Outline each blood parasite and name the species.
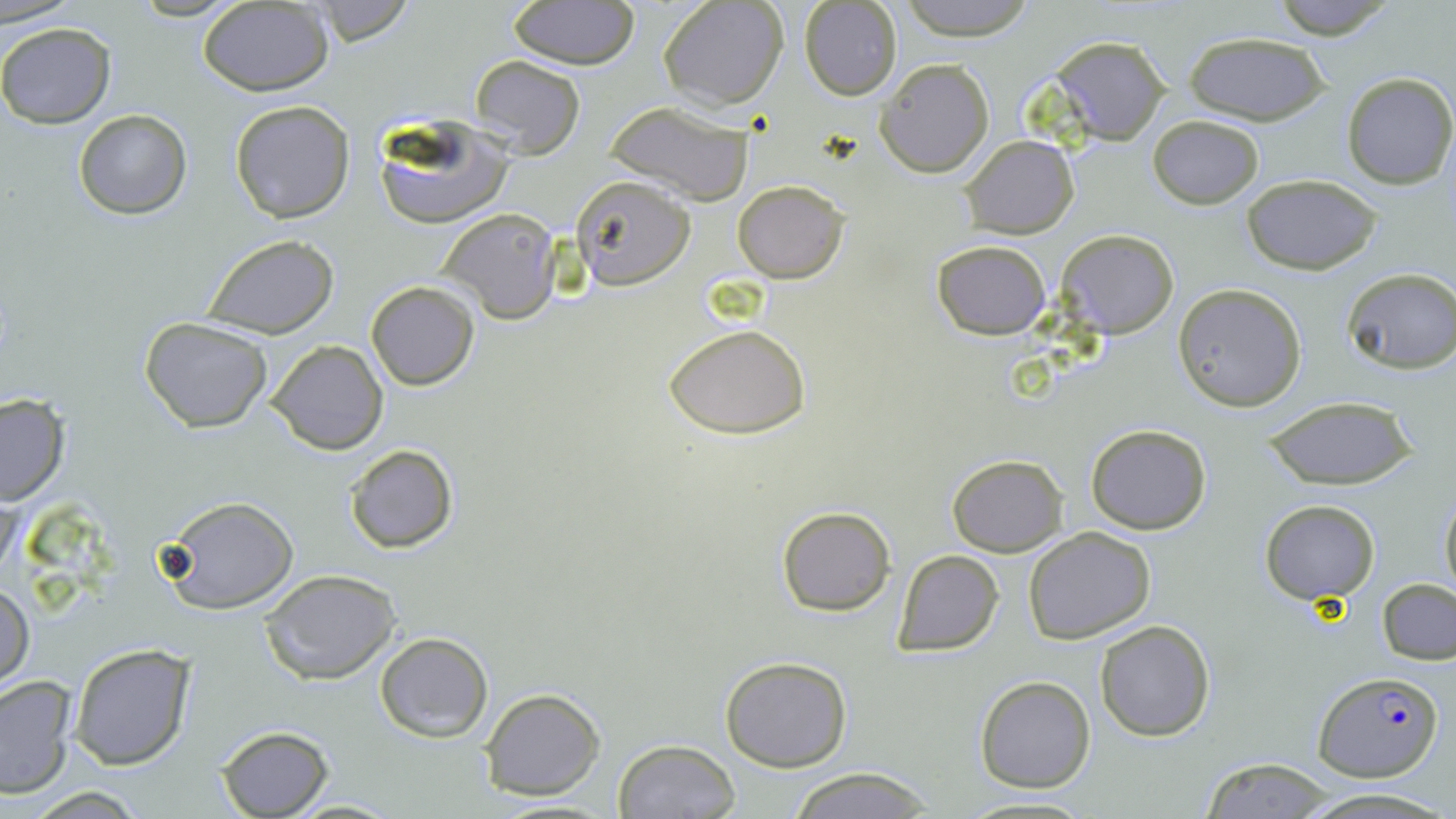

Approximate bounding boxes as (x1,y1)-(x2,y2) corner pairs in pixels.
Plasmodium falciparum-infected red blood cells: (1314,671)-(1444,782).
No Plasmodium ovale, Plasmodium malariae, Plasmodium vivax, Babesia divergens, or Trypanosoma brucei observed.

Summary:
  - Uninfected red blood cell locations: (3,0)-(79,26), (658,0)-(788,110), (896,0)-(1038,41), (1269,0)-(1398,40), (508,1)-(639,70), (798,1)-(902,99), (196,3)-(334,95), (0,22)-(115,128), (1182,33)-(1330,125), (1051,35)-(1171,144), (469,53)-(586,157), (874,58)-(995,178), (1340,71)-(1455,190), (229,99)-(356,223), (603,99)-(757,206), (73,108)-(192,221), (372,114)-(512,230), (1147,114)-(1264,208), (961,135)-(1078,237), (1241,174)-(1380,275), (572,175)-(696,289), (733,181)-(849,283), (438,208)-(562,324), (1057,229)-(1178,338), (202,235)-(340,338), (932,240)-(1051,338), (1342,269)-(1456,373), (366,281)-(480,391), (1173,284)-(1306,412), (139,316)-(274,433), (665,324)-(811,439), (268,340)-(386,455), (0,394)-(69,505), (1261,395)-(1419,490), (1086,423)-(1211,533), (344,443)-(458,554), (946,454)-(1067,557), (1439,483)-(1456,597), (156,494)-(299,614), (1259,499)-(1380,604), (775,505)-(897,617), (1022,527)-(1155,645), (893,549)-(1004,658), (260,569)-(399,684), (1378,578)-(1456,664), (1,582)-(35,692), (1095,619)-(1216,740), (374,631)-(493,742), (70,642)-(194,769), (719,655)-(852,772), (0,673)-(78,798), (974,675)-(1096,792), (479,687)-(606,802), (216,725)-(335,818), (613,740)-(740,819), (1196,758)-(1342,817), (783,767)-(939,819), (1300,787)-(1447,819), (283,796)-(401,817)
  - Slide-level diagnosis: Plasmodium falciparum
  - Magnification: 1000x
  - Modality: light microscopy
  - Stain: May-Grünwald-Giemsa
  - Preparation: thin blood smear
  - Field of view: single
  - Image size: 1456×819 pixels